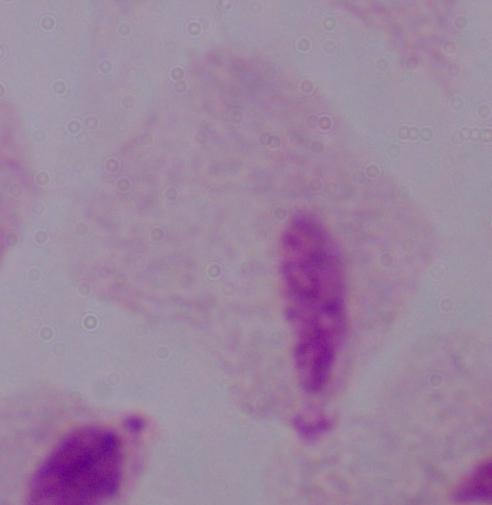

identification = trichomonad
modality = photomicrograph
magnification = 1000x